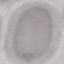

{
  "result": "negative for malaria parasites",
  "stain": "Giemsa",
  "capture": "smartphone camera at the microscope eyepiece",
  "preparation": "thin blood film",
  "image_type": "cell patch, automatically extracted from a larger field of view and resized to 64 × 64 pixels"
}